Assess this cell for malaria.
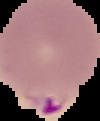

It is parasitized.

Image is 100×121 pixels. From a thin blood smear. Cell region segmented out of the field of view; the surrounding area is masked to black.